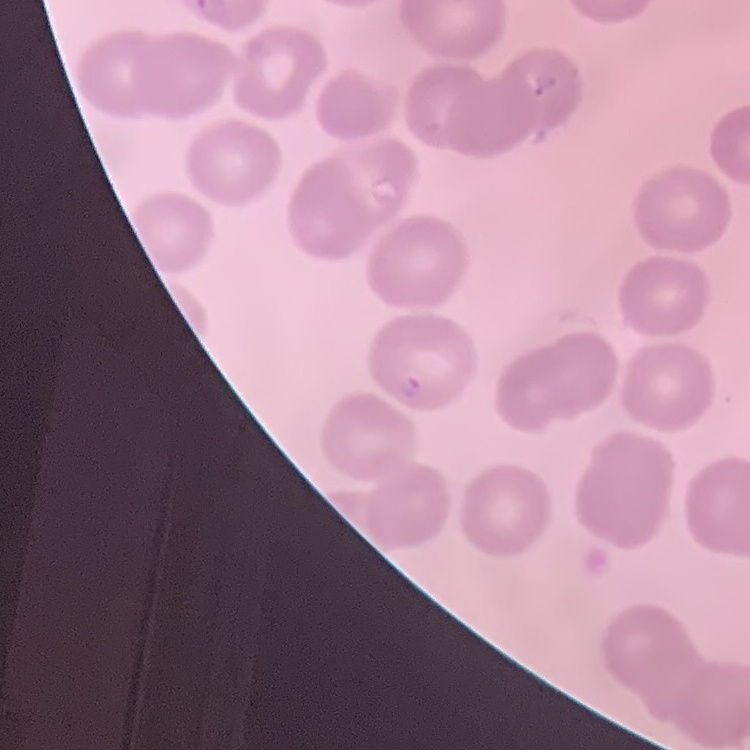
Summary:
  - Erythrocyte morphology: no rouleaux formation
  - Preparation: thin blood film
  - Stain: Field's or Giemsa
  - Image type: one tile cut from a larger photomicrograph